Report the malaria status of this cell.
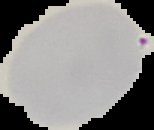
Uninfected.

{
  "image_size": "154×130 pixels",
  "preparation": "thin blood film",
  "image_type": "cell region segmented out of the field of view; surrounding area masked to black"
}